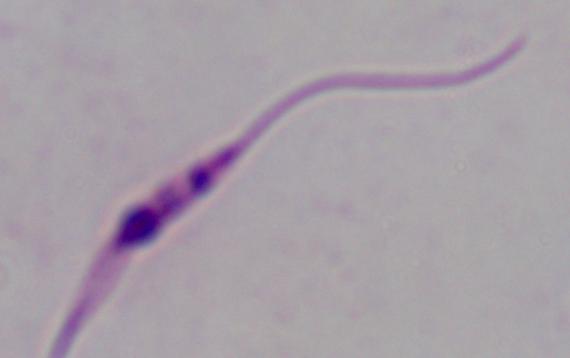 A Leishmania parasite is seen. Micrograph. Captured at 1000x magnification.